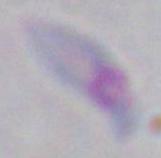

{
  "identification": "Toxoplasma gondii",
  "magnification": "1000x",
  "modality": "micrograph"
}